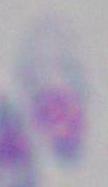

{
  "modality": "micrograph",
  "magnification": "1000x",
  "identification": "Toxoplasma gondii"
}